Assess the morphology of the red blood cells.
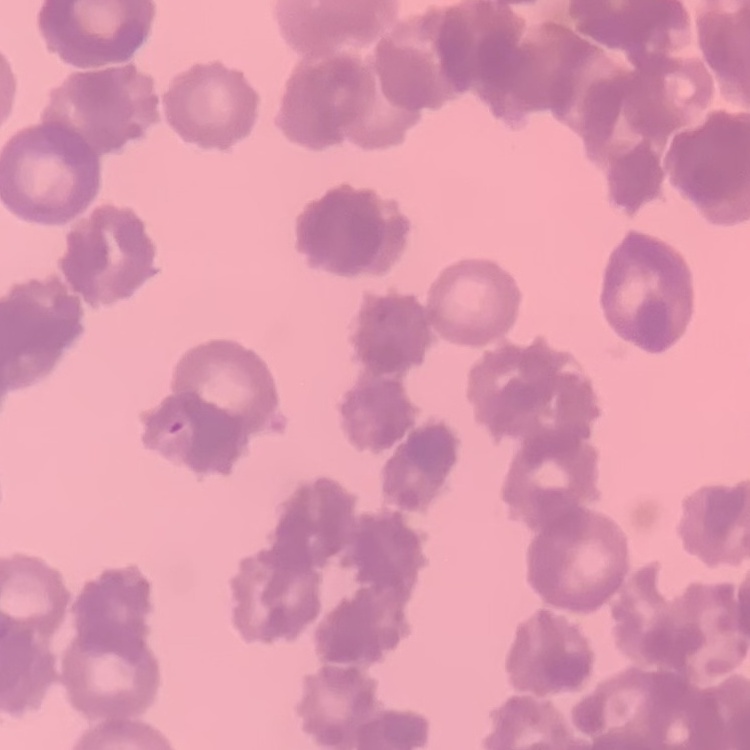

They show rouleaux formation.

Summary:
  - Image type: square crop of a larger photomicrograph
  - Stain: Field's or Giemsa
  - Preparation: thin blood smear